Classify this cell by malaria status.
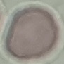
Uninfected.

Cell patch, automatically extracted from a larger field of view and resized to 64 × 64 pixels. Acquired by smartphone through the microscope eyepiece. Thin blood film. Giemsa-stained preparation.